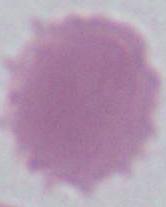
Summary:
  - Magnification: 1000x
  - Identification: red blood cell
  - Modality: micrograph